Name the blood parasite species.
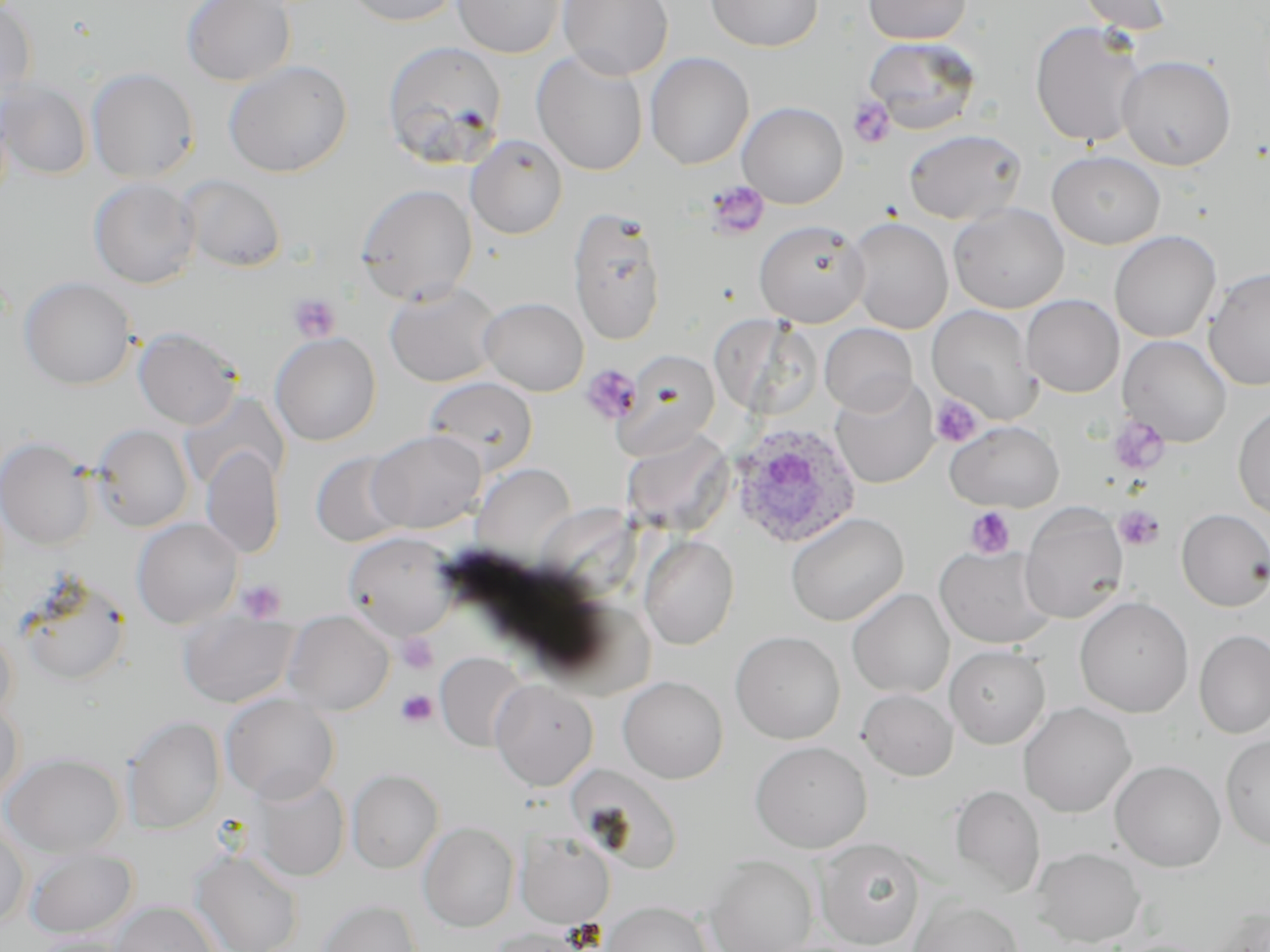
Plasmodium ovale.

{
  "modality": "light microscopy",
  "platelet_locations": "approximate bounding boxes as (x1, y1, x2, y2) in pixels: (848, 97, 896, 148), (705, 181, 771, 239), (288, 293, 341, 343), (582, 365, 642, 423), (930, 395, 983, 447), (1106, 415, 1170, 477), (1114, 505, 1165, 551), (964, 506, 1017, 558), (236, 579, 286, 623), (397, 633, 439, 674), (396, 689, 438, 728)",
  "stain": "May-Grünwald-Giemsa",
  "magnification": "1000x",
  "plasmodium_ovale_infected_red_blood_cell_locations": "approximate bounding boxes as (x1, y1, x2, y2) in pixels: (728, 422, 862, 549)",
  "field_of_view": "single",
  "image_size": "1270×952 pixels",
  "preparation": "thin blood film",
  "uninfected_red_blood_cell_locations": "approximate bounding boxes as (x1, y1, x2, y2) in pixels: (0, 0, 38, 103), (182, 0, 296, 86), (342, 0, 463, 26), (452, 0, 565, 58), (558, 0, 674, 80), (706, 0, 823, 52), (862, 0, 972, 44), (1075, 0, 1176, 35), (1030, 20, 1149, 148), (863, 37, 981, 135), (382, 41, 507, 168), (532, 51, 648, 176), (645, 52, 754, 169), (1116, 55, 1236, 171), (224, 60, 353, 178), (86, 67, 200, 183), (1, 79, 92, 180), (737, 101, 848, 209), (903, 128, 1027, 224), (465, 134, 568, 239), (1047, 150, 1166, 249), (178, 174, 287, 273), (88, 177, 200, 288), (355, 183, 478, 305), (948, 203, 1069, 313), (568, 207, 667, 345), (846, 217, 953, 334), (753, 220, 870, 327), (1109, 230, 1221, 343), (1204, 267, 1270, 391), (19, 277, 137, 390), (384, 281, 502, 386), (1021, 294, 1125, 397), (479, 297, 588, 396), (926, 305, 1042, 424), (820, 323, 918, 415), (133, 326, 242, 429), (270, 332, 381, 446), (1118, 335, 1232, 447), (618, 349, 720, 456), (829, 375, 939, 488), (423, 376, 538, 475), (1233, 403, 1270, 521), (945, 419, 1063, 512), (90, 424, 194, 532), (368, 429, 486, 533), (621, 430, 734, 534), (0, 436, 97, 550), (202, 445, 284, 559), (310, 451, 409, 547), (473, 463, 575, 561), (1020, 503, 1128, 624), (1176, 508, 1270, 611), (786, 512, 908, 626), (132, 518, 243, 628), (343, 531, 459, 641), (639, 535, 739, 649), (934, 543, 1056, 649), (16, 572, 132, 687), (847, 588, 954, 698), (1074, 596, 1194, 717), (283, 610, 394, 715), (178, 611, 299, 708), (0, 623, 18, 723), (1194, 629, 1270, 739), (730, 631, 846, 744), (945, 645, 1051, 748), (435, 652, 529, 752), (618, 675, 728, 783), (490, 680, 599, 790), (856, 688, 958, 781), (221, 692, 340, 804), (0, 696, 24, 805), (1018, 702, 1136, 818), (122, 716, 225, 834), (1221, 734, 1270, 851), (749, 740, 872, 853), (1, 753, 125, 857), (1110, 759, 1226, 872), (346, 768, 444, 873), (250, 775, 350, 881), (949, 784, 1046, 898), (0, 818, 30, 927), (419, 822, 519, 931), (516, 829, 616, 928), (815, 837, 926, 949), (24, 846, 138, 939), (1031, 846, 1146, 947), (191, 848, 304, 952), (704, 855, 818, 952), (317, 898, 422, 952), (908, 898, 1024, 952), (109, 901, 221, 952), (603, 901, 713, 952), (484, 927, 595, 952)"
}